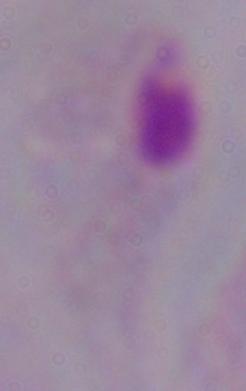
modality: micrograph
identification: trichomonad
magnification: 1000x